Report the malaria status of this cell.
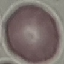
Uninfected.

Cell patch, automatically extracted from a larger field of view and resized to 64 × 64 pixels. Thin blood smear. Photographed with a smartphone camera at the microscope eyepiece. Giemsa-stained preparation.